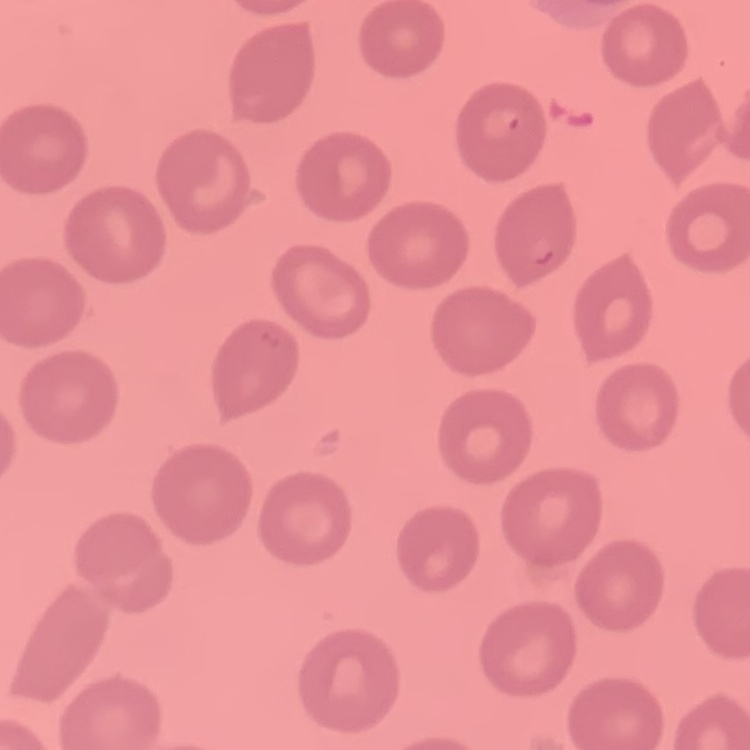

Summary:
  - Red blood cell morphology: no rouleaux formation
  - Image type: square crop of a larger photomicrograph
  - Preparation: thin blood smear
  - Stain: Field's or Giemsa